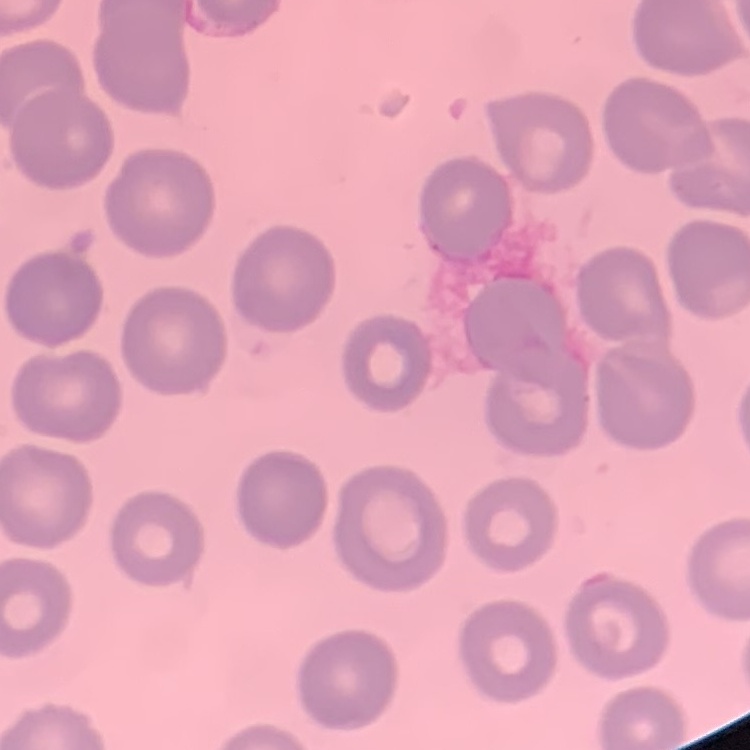

The erythrocytes show no rouleaux formation. Square crop of a larger photomicrograph. Stained with either Field's or Giemsa. Thin peripheral smear.